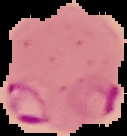
From a thin blood smear. Image is 127×136 pixels. The area outside the segmented cell region is set to black. Malaria status: parasitized.